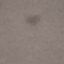

result = negative for malaria parasites
image type = automatically extracted cell patch, resized to 64 × 64 pixels
preparation = thin smear
capture = smartphone camera at the microscope eyepiece
stain = Giemsa